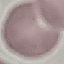

Summary:
  - Malaria status: uninfected
  - Image type: cell patch, automatically extracted from a larger field of view and resized to 64 × 64 pixels
  - Capture: smartphone through the microscope eyepiece
  - Stain: Giemsa
  - Preparation: thin blood smear